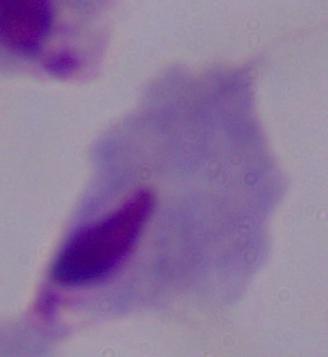
Captured at 1000x magnification. A trichomonad is shown. Photomicrograph.